Classify this cell by malaria status.
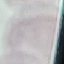

It is uninfected.

Giemsa stain. Thin blood smear. Photographed with a smartphone camera at the microscope eyepiece. Automatically extracted cell patch, resized to 64 × 64 pixels.